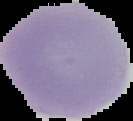 Image is 133×121 pixels. Cell region segmented out of the field of view; the surrounding area is masked to black. Result: no malaria parasites seen. From a thin blood smear.